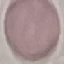
Summary:
  - Malaria status: uninfected
  - Stain: Giemsa
  - Capture: smartphone camera at the microscope eyepiece
  - Preparation: thin smear
  - Image type: automatically extracted cell patch, resized to 64 × 64 pixels